Outline each blood parasite and name the species.
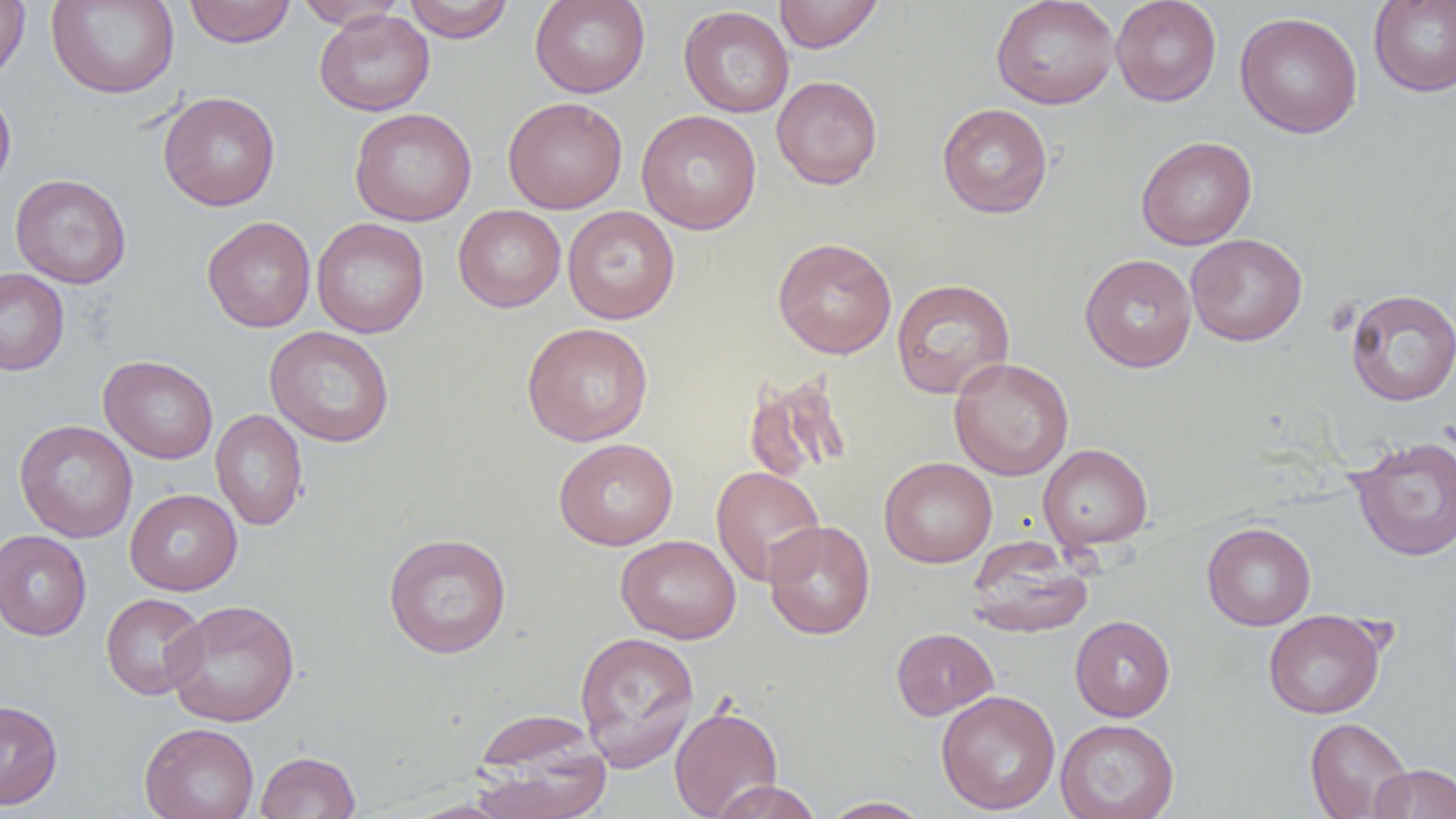

No blood parasites observed.

Approximate bounding boxes as named x1/y1/x2/y2 corners in pixels. Uninfected red blood cell locations: (x1=0, y1=0, x2=31, y2=83), (x1=46, y1=0, x2=180, y2=99), (x1=293, y1=0, x2=407, y2=28), (x1=403, y1=0, x2=514, y2=43), (x1=530, y1=0, x2=650, y2=98), (x1=774, y1=0, x2=884, y2=53), (x1=991, y1=0, x2=1120, y2=109), (x1=1111, y1=0, x2=1222, y2=106), (x1=1369, y1=0, x2=1456, y2=97), (x1=183, y1=1, x2=296, y2=48), (x1=678, y1=5, x2=794, y2=117), (x1=314, y1=9, x2=434, y2=116), (x1=1235, y1=11, x2=1363, y2=139), (x1=771, y1=75, x2=883, y2=190), (x1=0, y1=85, x2=16, y2=196), (x1=158, y1=91, x2=281, y2=211), (x1=503, y1=96, x2=628, y2=213), (x1=937, y1=102, x2=1053, y2=218), (x1=349, y1=107, x2=477, y2=226), (x1=636, y1=110, x2=762, y2=234), (x1=1136, y1=136, x2=1257, y2=250), (x1=10, y1=173, x2=131, y2=289), (x1=453, y1=204, x2=566, y2=312), (x1=562, y1=206, x2=680, y2=324), (x1=202, y1=216, x2=316, y2=332), (x1=312, y1=218, x2=429, y2=339), (x1=1186, y1=233, x2=1307, y2=346), (x1=772, y1=237, x2=897, y2=359), (x1=1080, y1=253, x2=1197, y2=372), (x1=0, y1=268, x2=70, y2=376), (x1=890, y1=278, x2=1015, y2=399), (x1=1345, y1=289, x2=1456, y2=406), (x1=521, y1=322, x2=654, y2=446), (x1=264, y1=326, x2=395, y2=447), (x1=99, y1=355, x2=218, y2=464), (x1=949, y1=357, x2=1074, y2=481), (x1=742, y1=373, x2=852, y2=484), (x1=210, y1=409, x2=308, y2=531), (x1=14, y1=419, x2=138, y2=543), (x1=1349, y1=435, x2=1456, y2=562), (x1=553, y1=437, x2=679, y2=550), (x1=1038, y1=443, x2=1154, y2=551), (x1=879, y1=457, x2=997, y2=568), (x1=711, y1=466, x2=825, y2=586), (x1=125, y1=488, x2=242, y2=595), (x1=762, y1=519, x2=875, y2=640), (x1=1202, y1=522, x2=1316, y2=631), (x1=0, y1=529, x2=92, y2=641), (x1=383, y1=532, x2=512, y2=658), (x1=615, y1=534, x2=742, y2=644), (x1=966, y1=539, x2=1093, y2=638), (x1=101, y1=593, x2=208, y2=700), (x1=165, y1=599, x2=301, y2=727), (x1=1263, y1=609, x2=1387, y2=718), (x1=1070, y1=615, x2=1175, y2=721), (x1=891, y1=627, x2=999, y2=720), (x1=573, y1=630, x2=700, y2=770), (x1=936, y1=689, x2=1060, y2=815), (x1=0, y1=700, x2=63, y2=810), (x1=669, y1=705, x2=783, y2=819), (x1=1304, y1=717, x2=1413, y2=819), (x1=1055, y1=718, x2=1180, y2=819), (x1=140, y1=722, x2=259, y2=819), (x1=470, y1=722, x2=612, y2=819), (x1=255, y1=750, x2=361, y2=819), (x1=1369, y1=763, x2=1456, y2=818), (x1=709, y1=780, x2=823, y2=818), (x1=819, y1=796, x2=933, y2=818), (x1=403, y1=799, x2=518, y2=819). Slide-level diagnosis: no evidence of blood parasites. 1000x magnification. Single field of view. Image is 1456×819 pixels. Thin blood film. Light microscopy.